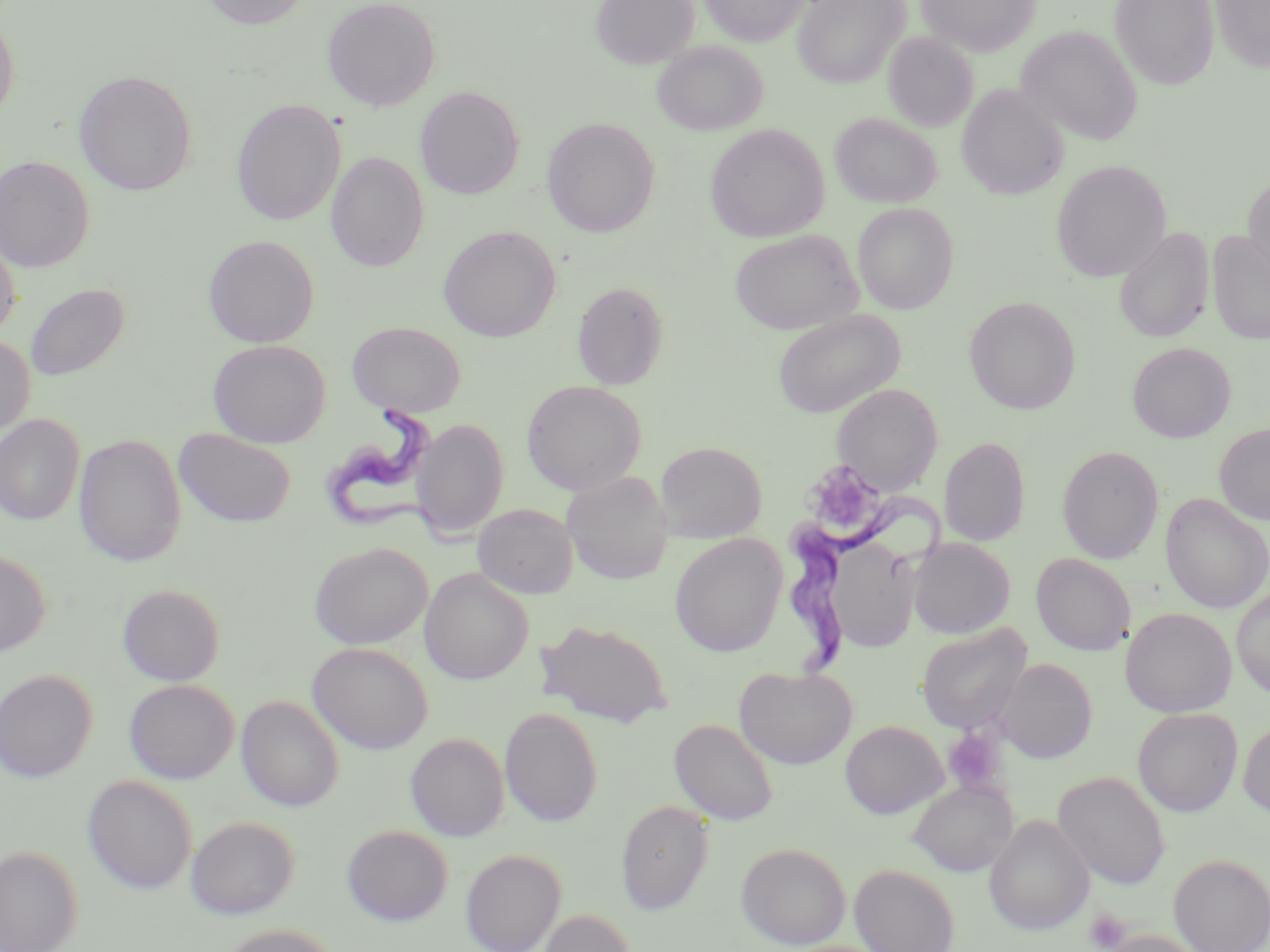
slide-level diagnosis = Trypanosoma brucei
uninfected red blood cell locations = approximate bounding boxes as named x1/y1/x2/y2 corners in pixels: (x1=199, y1=0, x2=313, y2=30), (x1=322, y1=0, x2=441, y2=111), (x1=590, y1=0, x2=699, y2=69), (x1=700, y1=0, x2=808, y2=47), (x1=794, y1=0, x2=909, y2=88), (x1=916, y1=0, x2=1039, y2=57), (x1=1110, y1=0, x2=1219, y2=90), (x1=1211, y1=1, x2=1270, y2=73), (x1=0, y1=9, x2=20, y2=123), (x1=1015, y1=25, x2=1142, y2=146), (x1=883, y1=32, x2=978, y2=133), (x1=652, y1=41, x2=768, y2=136), (x1=73, y1=70, x2=197, y2=196), (x1=957, y1=84, x2=1068, y2=200), (x1=415, y1=87, x2=524, y2=199), (x1=231, y1=99, x2=345, y2=226), (x1=830, y1=112, x2=942, y2=208), (x1=541, y1=117, x2=659, y2=237), (x1=704, y1=123, x2=830, y2=243), (x1=326, y1=152, x2=429, y2=272), (x1=0, y1=155, x2=94, y2=272), (x1=1051, y1=160, x2=1170, y2=283), (x1=1242, y1=173, x2=1270, y2=280), (x1=852, y1=202, x2=959, y2=314), (x1=439, y1=225, x2=560, y2=342), (x1=1115, y1=227, x2=1214, y2=343), (x1=729, y1=229, x2=862, y2=335), (x1=1207, y1=230, x2=1270, y2=345), (x1=0, y1=234, x2=21, y2=339), (x1=203, y1=235, x2=319, y2=347), (x1=573, y1=281, x2=668, y2=390), (x1=25, y1=283, x2=129, y2=381), (x1=964, y1=296, x2=1080, y2=414), (x1=772, y1=309, x2=906, y2=418), (x1=347, y1=321, x2=465, y2=416), (x1=0, y1=335, x2=35, y2=437), (x1=208, y1=339, x2=330, y2=447), (x1=1127, y1=342, x2=1235, y2=442), (x1=522, y1=380, x2=647, y2=495), (x1=832, y1=383, x2=943, y2=495), (x1=0, y1=414, x2=85, y2=525), (x1=412, y1=418, x2=509, y2=540), (x1=1214, y1=422, x2=1270, y2=525), (x1=174, y1=429, x2=296, y2=527), (x1=73, y1=434, x2=186, y2=567), (x1=939, y1=437, x2=1030, y2=547), (x1=655, y1=441, x2=767, y2=542), (x1=1056, y1=445, x2=1164, y2=564), (x1=561, y1=471, x2=673, y2=585), (x1=1161, y1=493, x2=1270, y2=614), (x1=472, y1=504, x2=578, y2=599), (x1=669, y1=533, x2=787, y2=657), (x1=822, y1=537, x2=921, y2=654), (x1=908, y1=537, x2=1015, y2=639), (x1=309, y1=542, x2=432, y2=649), (x1=0, y1=550, x2=50, y2=656), (x1=1031, y1=552, x2=1135, y2=655), (x1=419, y1=568, x2=533, y2=685), (x1=117, y1=584, x2=225, y2=686), (x1=1232, y1=587, x2=1270, y2=699), (x1=1120, y1=607, x2=1236, y2=717), (x1=536, y1=619, x2=673, y2=728), (x1=917, y1=622, x2=1032, y2=734), (x1=308, y1=642, x2=432, y2=754), (x1=994, y1=658, x2=1097, y2=763), (x1=734, y1=665, x2=857, y2=770), (x1=0, y1=669, x2=97, y2=782), (x1=124, y1=679, x2=239, y2=784), (x1=236, y1=695, x2=344, y2=812), (x1=499, y1=708, x2=602, y2=826), (x1=1132, y1=708, x2=1242, y2=817), (x1=669, y1=719, x2=778, y2=825), (x1=840, y1=720, x2=947, y2=818), (x1=1238, y1=720, x2=1270, y2=818), (x1=406, y1=733, x2=509, y2=842), (x1=1053, y1=770, x2=1171, y2=889), (x1=82, y1=775, x2=197, y2=894), (x1=907, y1=779, x2=1018, y2=877), (x1=616, y1=800, x2=714, y2=914), (x1=984, y1=815, x2=1095, y2=935), (x1=186, y1=816, x2=299, y2=919), (x1=342, y1=824, x2=453, y2=926), (x1=736, y1=842, x2=851, y2=949), (x1=0, y1=846, x2=82, y2=952), (x1=461, y1=849, x2=566, y2=952), (x1=1168, y1=853, x2=1270, y2=952), (x1=849, y1=863, x2=959, y2=952), (x1=537, y1=909, x2=634, y2=952), (x1=217, y1=924, x2=342, y2=952), (x1=1102, y1=930, x2=1207, y2=952)
modality = optical microscopy
stain = May-Grünwald-Giemsa
platelet locations = approximate bounding boxes as named x1/y1/x2/y2 corners in pixels: (x1=801, y1=460, x2=888, y2=540), (x1=943, y1=727, x2=1008, y2=796), (x1=1085, y1=909, x2=1130, y2=950)
field of view = one of a larger specimen
preparation = thin blood film
Trypanosoma brucei locations = approximate bounding boxes as named x1/y1/x2/y2 corners in pixels: (x1=320, y1=402, x2=451, y2=547), (x1=786, y1=488, x2=945, y2=673)
magnification = 1000x
image size = 1270×952 pixels